Describe the morphology of the erythrocytes.
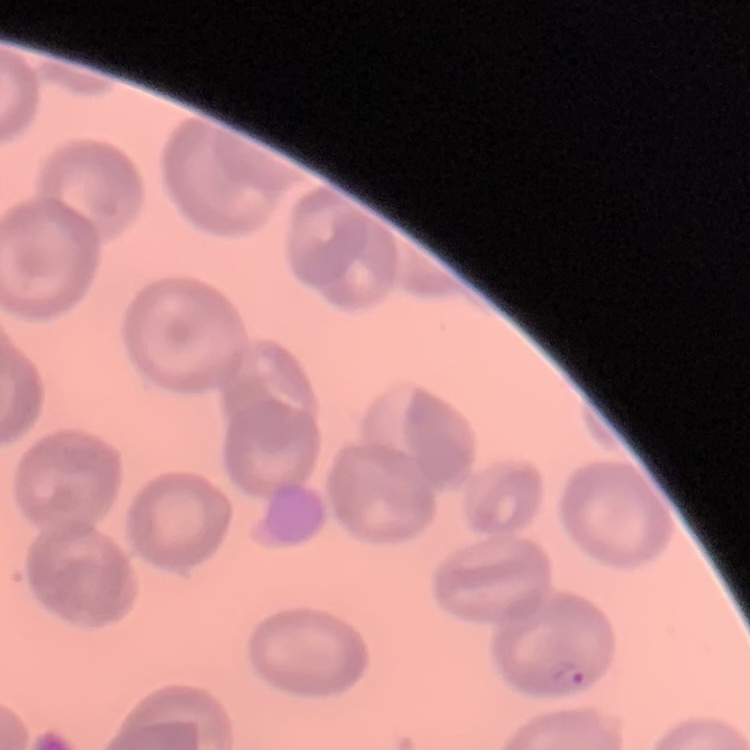

No rouleaux formation.

Thin blood smear. Field's or Giemsa stain. Square crop of a larger photomicrograph.